Assess the morphology of the red blood cells.
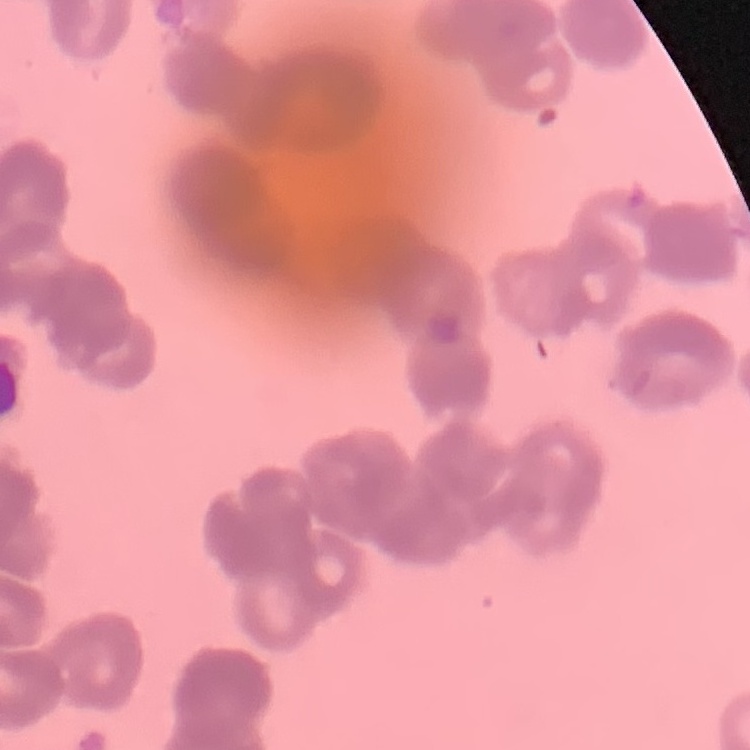
Rouleaux formation.

Square crop of a larger photomicrograph. Field's or Giemsa stain. Thin peripheral smear.